State which parasite is depicted.
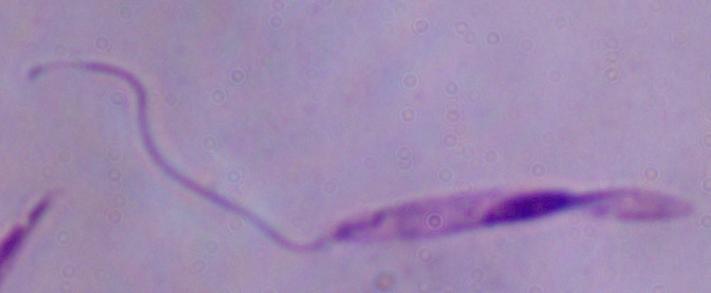

This is Leishmania.

1000x magnification. Micrograph.